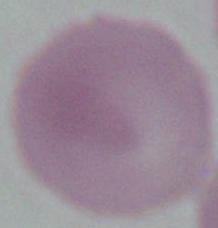
Summary:
  - Identification: red blood cell
  - Magnification: 1000x
  - Modality: micrograph